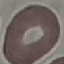
Summary:
  - Result: no malaria parasites detected
  - Capture: smartphone through the microscope eyepiece
  - Stain: Giemsa
  - Preparation: thin smear
  - Image type: automatically extracted cell patch, resized to 64 × 64 pixels